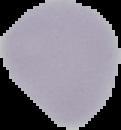
Summary:
  - Preparation: thin blood smear
  - Result: negative for malaria parasites
  - Image type: segmented cell region on a black background
  - Image size: 121×130 pixels